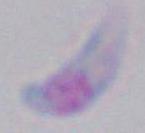
Summary:
  - Modality: photomicrograph
  - Magnification: 1000x
  - Identification: Toxoplasma gondii